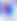

Captured at 400x magnification. Toxoplasma gondii is seen. Micrograph.